Name the parasite shown.
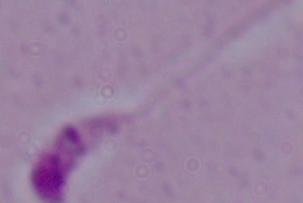

This is Leishmania.

{
  "modality": "photomicrograph",
  "magnification": "1000x"
}